Give the position of every Plasmodium parasite visible.
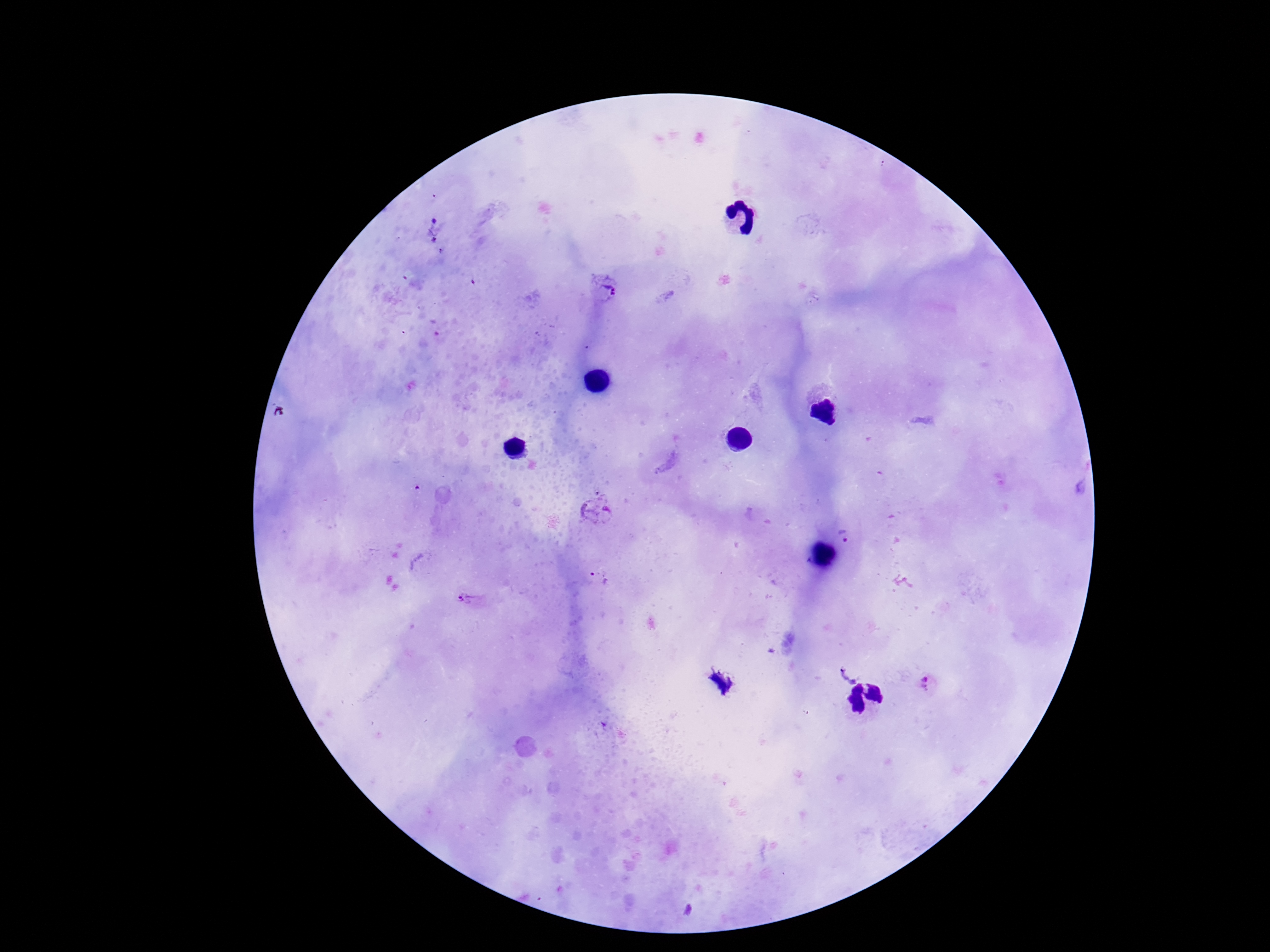

Approximate centers as {x, y} in pixels.
Plasmodium parasites: {437, 233}, {607, 292}, {598, 511}, {849, 536}, {598, 581}, {467, 600}, {846, 675}, {929, 683}.

preparation = thick peripheral-blood smear
stain = Giemsa
magnification = 100x
field of view = single
capture = smartphone camera through the microscope eyepiece
patient malaria status = infected
image size = 1270×952 pixels